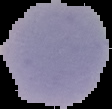
From a thin blood film. Result: no Plasmodium parasites seen. Image is 112×109 pixels. Cell region segmented out of the field of view; the surrounding area is masked to black.